Report the malaria status of this cell.
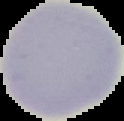
Uninfected.

The area outside the segmented cell region is set to black. From a thin blood film. Image is 124×121 pixels.